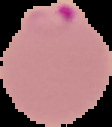
Summary:
  - Malaria status: parasitized
  - Image size: 112×127 pixels
  - Preparation: thin blood film
  - Image type: segmented cell region on a black background